Report the malaria status of this cell.
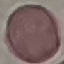
Uninfected.

Thin blood film. Automatically extracted cell patch, resized to 64 × 64 pixels. Acquired by smartphone through the microscope eyepiece. Giemsa-stained preparation.